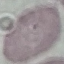

result = negative for malaria parasites
image type = automatically extracted cell patch, resized to 64 × 64 pixels
capture = smartphone through the microscope eyepiece
preparation = thin blood smear
stain = Giemsa